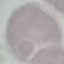

result = no malaria parasites detected
capture = smartphone through the microscope eyepiece
image type = automatically extracted cell patch, resized to 64 × 64 pixels
preparation = thin blood film
stain = Giemsa